Assess for Plasmodium parasites.
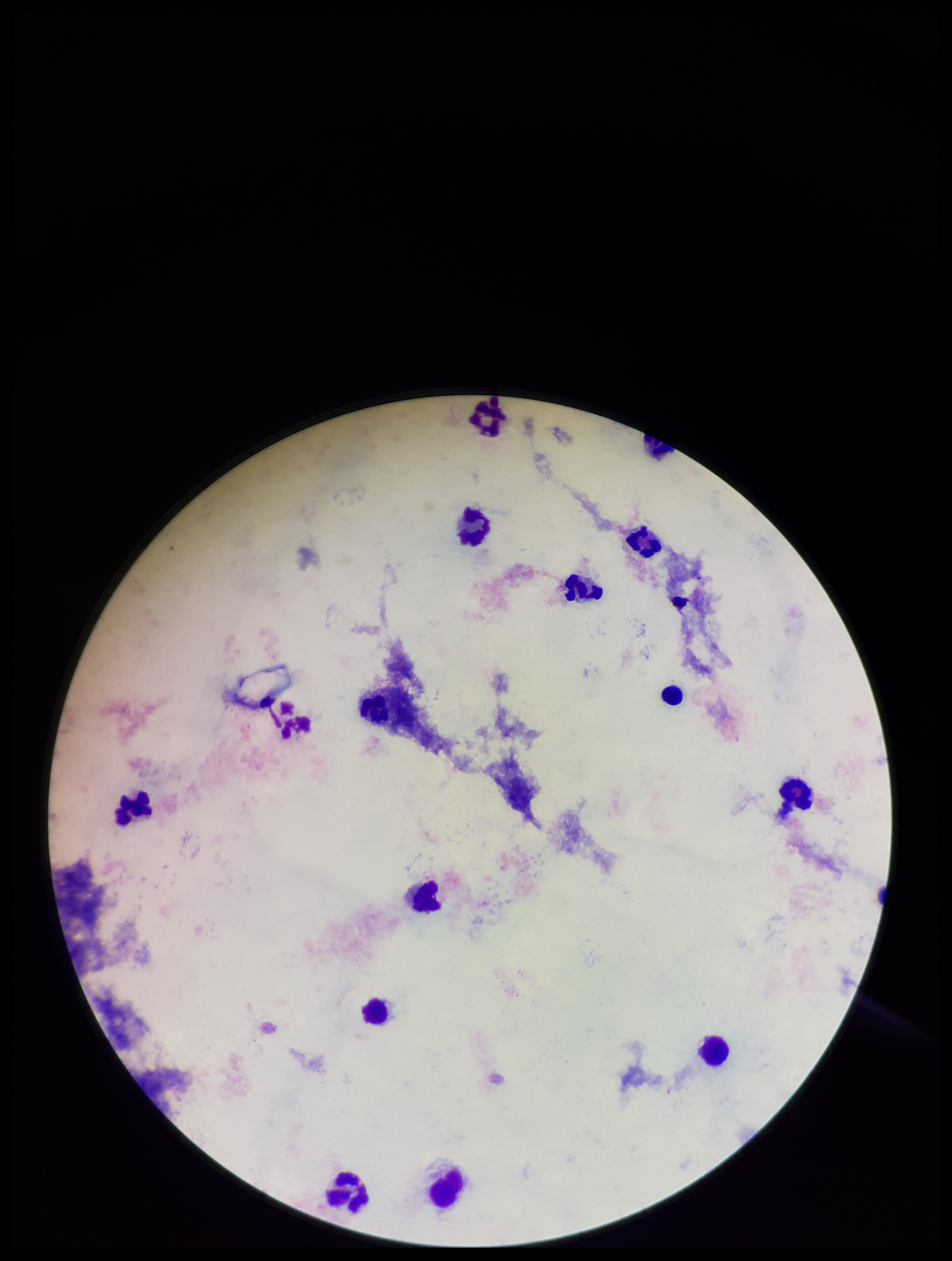
None seen.

Single field of view. Image is 952×1261 pixels. Leukocyte count: 14. Patient malaria status: negative. Stained with Giemsa. Parasite count: 0. Preparation: thick blood smear. Photographed through the microscope eyepiece with a smartphone camera.